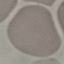

malaria status = uninfected
stain = Giemsa
preparation = thin blood smear
capture = smartphone camera at the microscope eyepiece
image type = cell patch, automatically extracted from a larger field of view and resized to 64 × 64 pixels